Outline each blood parasite and name the species.
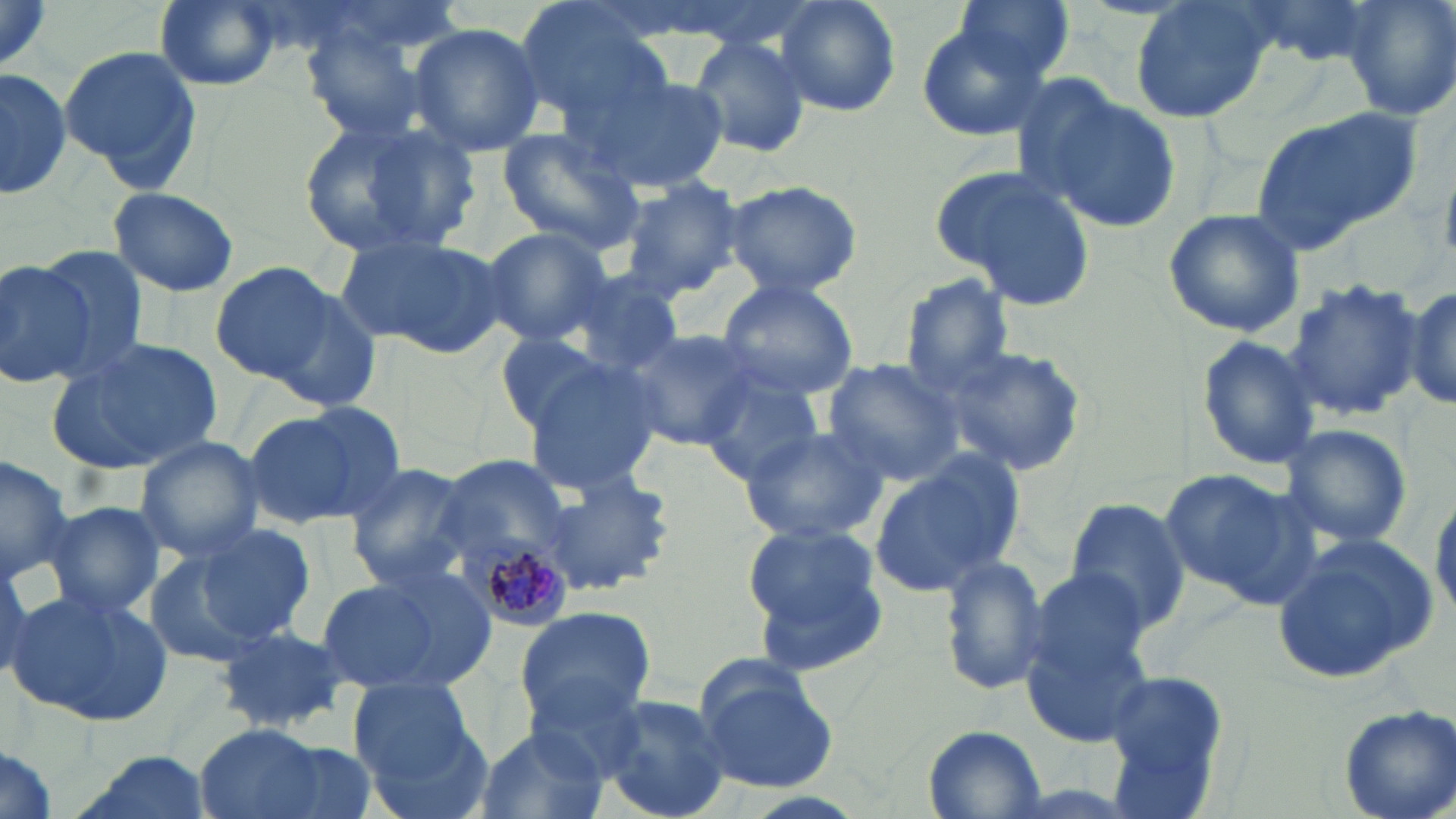
Approximate bounding boxes as (x1,y1)-(x2,y2) corner pairs in pixels.
Plasmodium malariae-infected red blood cells: (456,532)-(570,634).
No Plasmodium falciparum, Plasmodium ovale, Plasmodium vivax, Babesia divergens, or Trypanosoma brucei observed.

Summary:
  - Uninfected red blood cell locations: (0,0)-(56,81), (154,0)-(282,90), (772,0)-(902,117), (951,0)-(1077,86), (1129,0)-(1275,125), (1346,0)-(1456,121), (513,1)-(672,125), (406,23)-(547,157), (916,24)-(1051,139), (304,32)-(434,142), (689,34)-(812,158), (57,44)-(203,191), (1,66)-(71,203), (583,71)-(731,195), (1023,83)-(1182,231), (1248,108)-(1422,252), (298,115)-(479,259), (496,126)-(647,256), (929,164)-(1097,309), (619,178)-(745,298), (722,179)-(865,297), (109,185)-(239,297), (1164,207)-(1307,338), (474,227)-(613,349), (336,230)-(508,358), (34,247)-(149,377), (0,258)-(94,390), (209,261)-(344,386), (561,267)-(688,376), (897,273)-(1019,391), (1281,277)-(1426,421), (254,278)-(385,411), (717,279)-(858,399), (1399,281)-(1456,414), (621,327)-(760,450), (499,331)-(614,433), (1195,334)-(1324,470), (52,335)-(223,474), (936,344)-(1088,476), (520,356)-(664,495), (821,358)-(963,486), (701,371)-(827,487), (240,403)-(398,532), (1276,423)-(1414,550), (740,425)-(889,544), (134,436)-(265,562), (0,450)-(75,579), (868,450)-(1026,598), (433,451)-(583,591), (343,462)-(477,590), (1158,468)-(1303,598), (539,469)-(675,596), (1431,489)-(1456,621), (1061,495)-(1194,635), (42,500)-(165,622), (741,518)-(889,662), (194,523)-(317,644), (1272,537)-(1439,685), (140,546)-(263,666), (936,553)-(1051,695), (0,559)-(37,683), (1023,567)-(1152,682), (311,577)-(452,694), (7,584)-(171,724), (514,607)-(656,730), (214,621)-(353,734), (1021,626)-(1156,746), (517,669)-(653,776), (1103,669)-(1232,795), (696,670)-(838,791), (348,674)-(479,789), (597,693)-(736,819), (1338,704)-(1456,819), (194,723)-(344,819), (923,726)-(1046,817), (474,727)-(609,819), (0,745)-(58,819), (63,752)-(215,819)
  - Slide-level diagnosis: Plasmodium malariae
  - Image size: 1456×819 pixels
  - Field of view: single
  - Stain: May-Grünwald-Giemsa
  - Modality: optical microscopy
  - Preparation: thin blood smear
  - Magnification: 1000x